State which cell type is depicted.
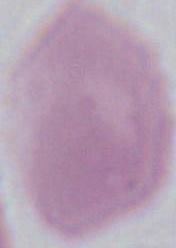

This is an erythrocyte.

Summary:
  - Magnification: 1000x
  - Modality: micrograph